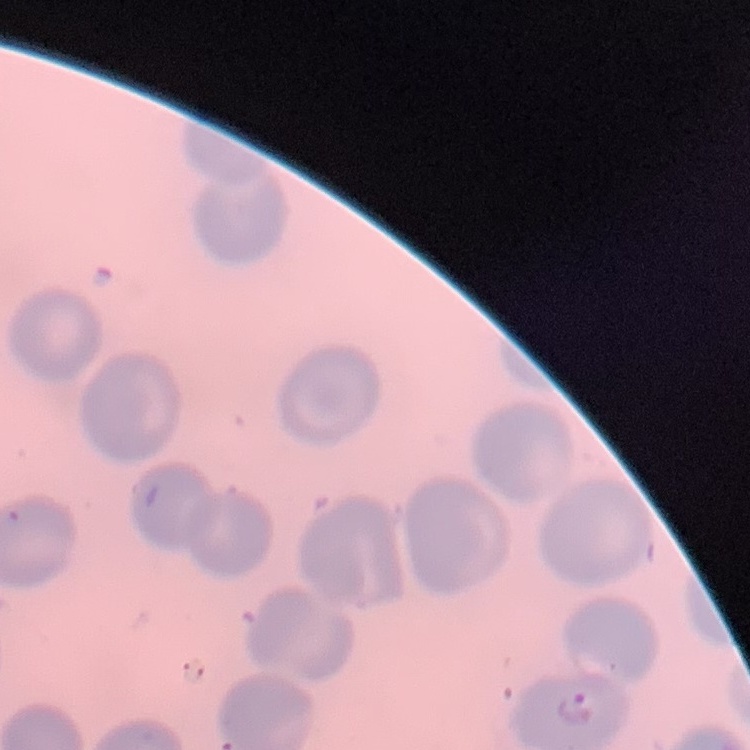

{
  "red_blood_cell_morphology": "no rouleaux formation",
  "image_type": "square crop of a larger photomicrograph",
  "preparation": "thin blood smear",
  "stain": "Field's or Giemsa"
}